Report the malaria status of this cell.
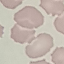

It is uninfected.

Summary:
  - Stain: Giemsa
  - Capture: smartphone camera at the microscope eyepiece
  - Image type: automatically extracted cell patch, resized to 64 × 64 pixels
  - Preparation: thin smear